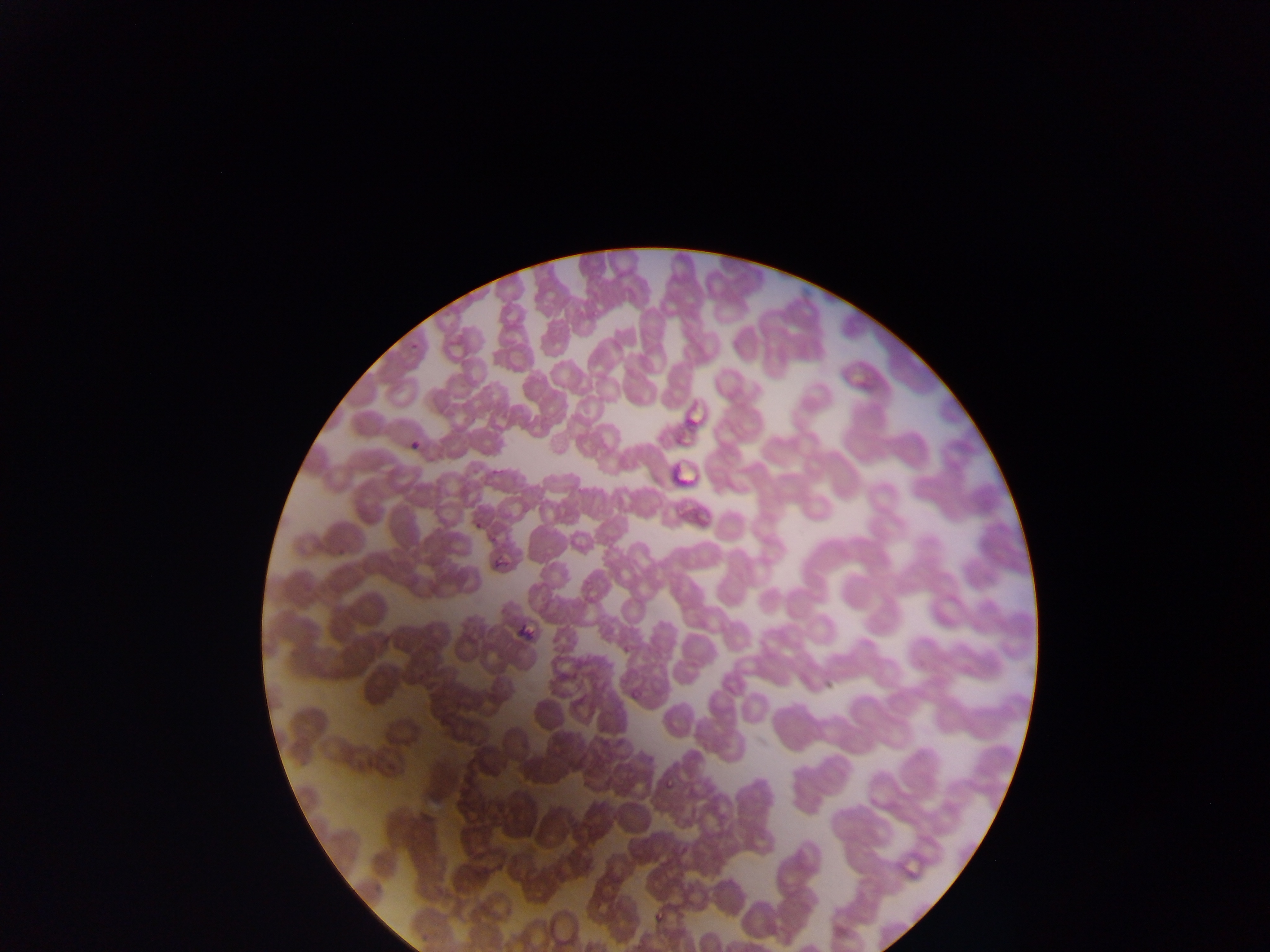 Approximate bounding boxes as (left, top, right, bottom) in pixels. Malaria parasite locations: (621, 641, 634, 650), (630, 687, 639, 699), (665, 776, 676, 790), (655, 910, 665, 921). Image is 1270×952 pixels. Thin blood film. Sample from Ghana. Single field of view. Photographed through a microscope with a mobile-phone camera.